Name the parasite shown.
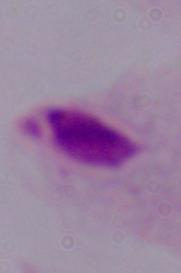
This is a trichomonad.

Summary:
  - Magnification: 1000x
  - Modality: photomicrograph